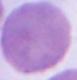
1000x magnification. Micrograph. An erythrocyte is seen.